Assess the morphology of the red blood cells.
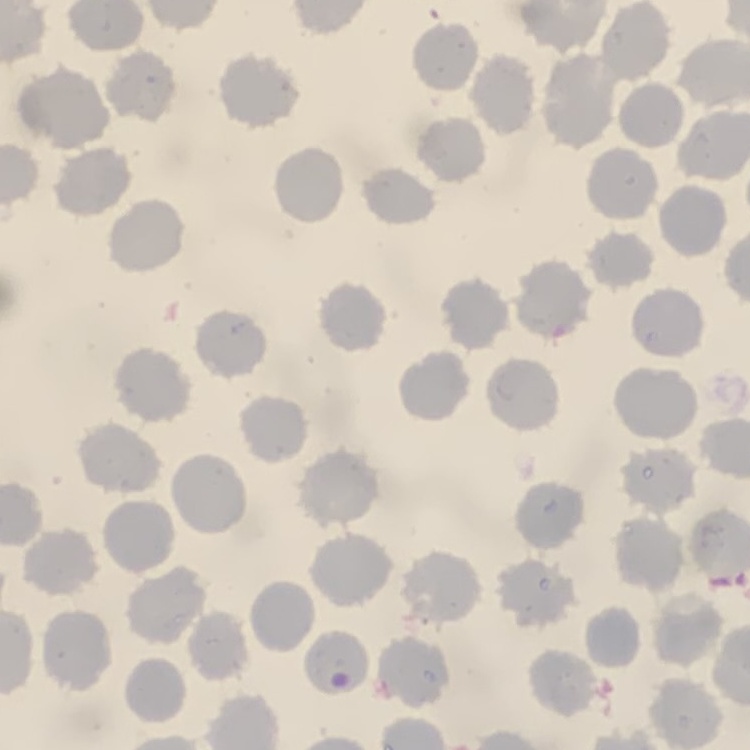
No rouleaux formation.

Summary:
  - Preparation: thin peripheral smear
  - Image type: one tile cut from a larger photomicrograph
  - Stain: Field's or Giemsa